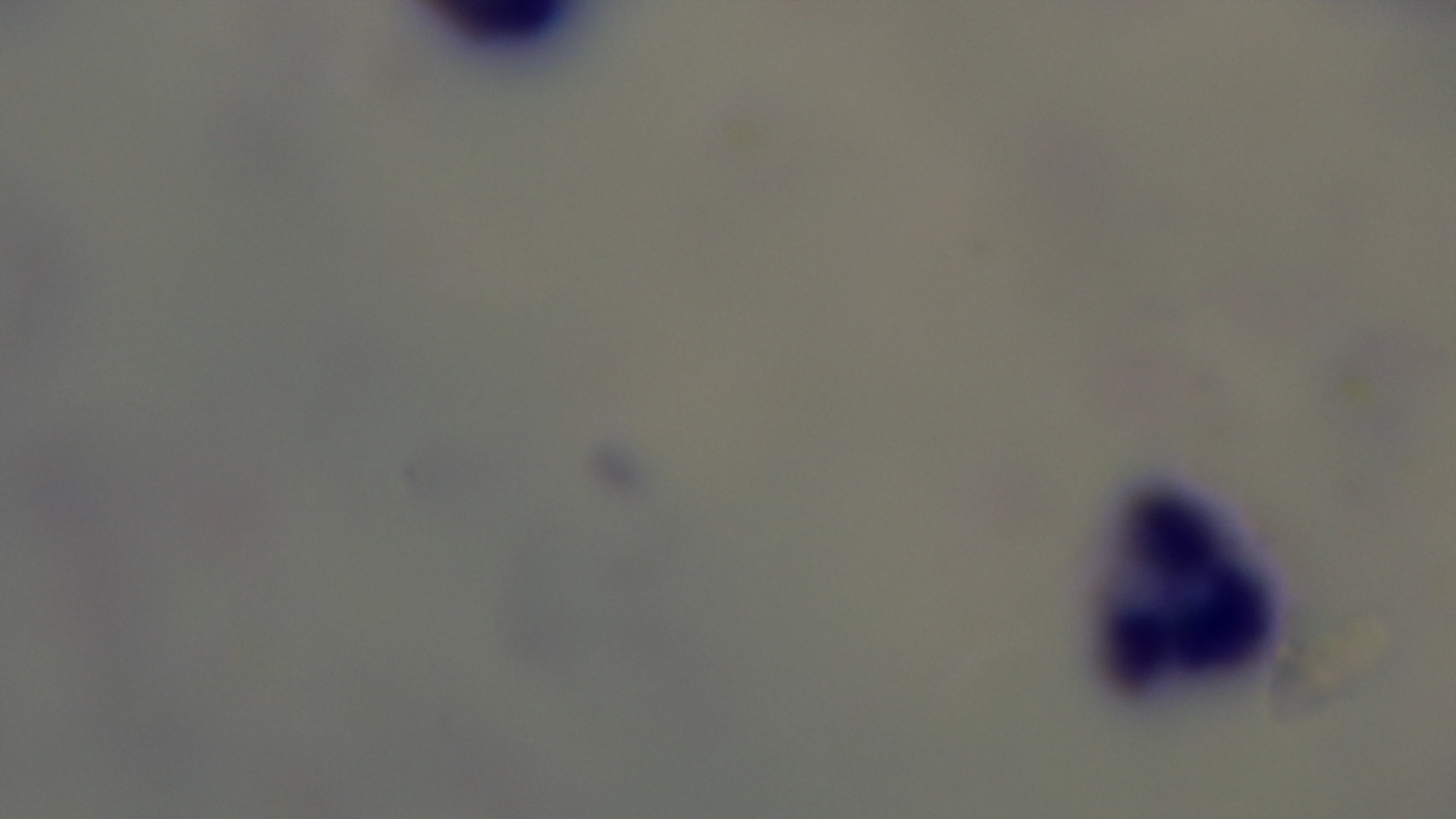

Summary:
  - Capture: mounted 4K digital camera
  - Modality: light microscopy
  - Stain: Giemsa
  - Preparation: thick smear
  - Field of view: single
  - Malaria status: uninfected
  - Objective: 100x oil immersion